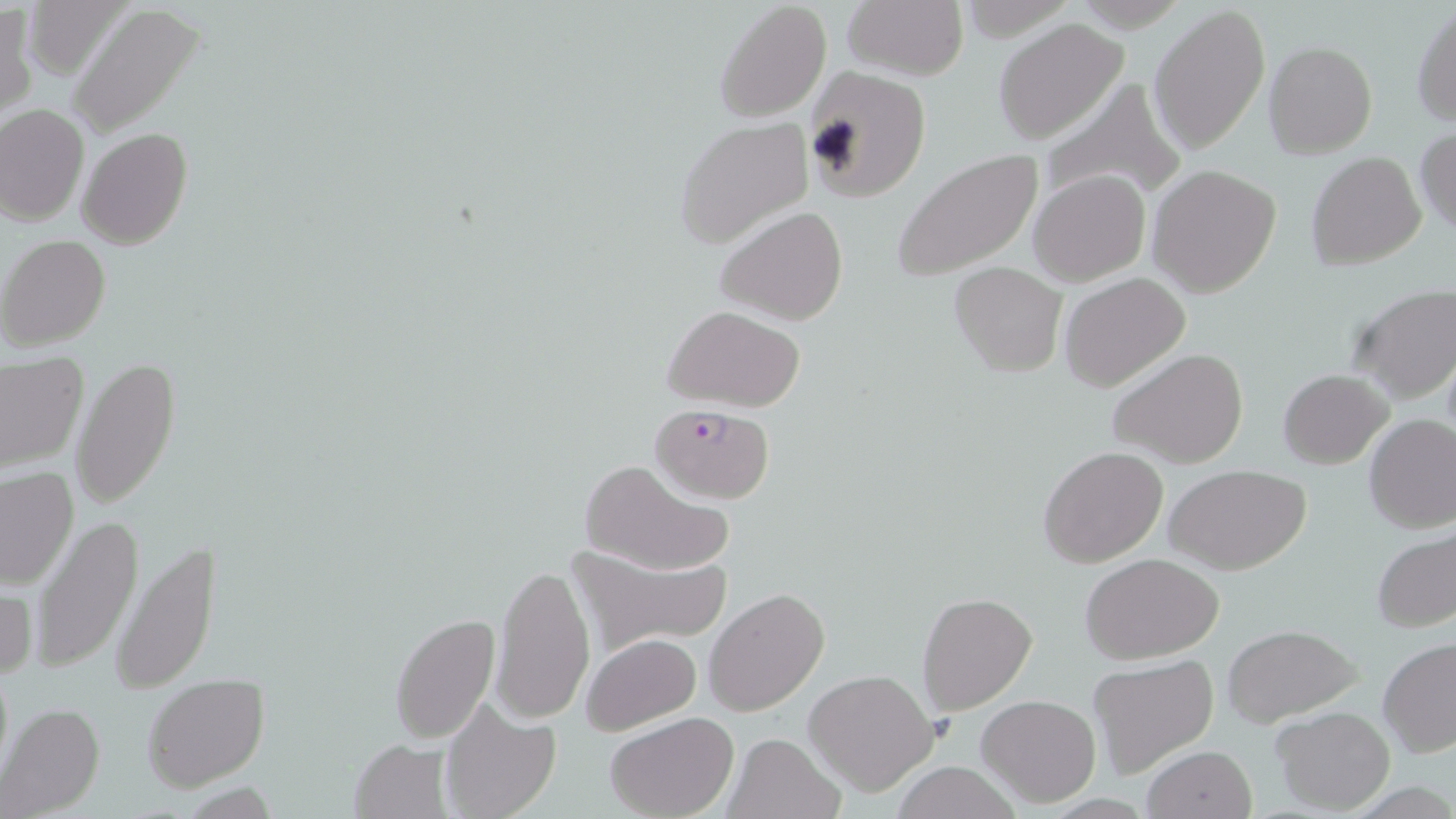

Summary:
  - Coordinate format: approximate bounding boxes as (x1,y1)-(x2,y2) corner pairs in pixels
  - Plasmodium falciparum-infected red blood cell locations: (651,403)-(776,503)
  - Uninfected red blood cell locations: (714,0)-(832,120), (842,1)-(968,81), (1150,3)-(1270,156), (1,4)-(35,122), (68,4)-(205,138), (1411,5)-(1456,126), (992,18)-(1129,144), (1263,41)-(1377,159), (799,66)-(931,204), (1033,76)-(1189,208), (0,104)-(88,224), (675,117)-(815,252), (1414,126)-(1456,237), (78,127)-(193,249), (892,149)-(1044,282), (1306,152)-(1427,270), (1147,164)-(1282,297), (1027,171)-(1151,285), (716,205)-(848,325), (1,236)-(112,352), (949,262)-(1066,378), (1059,273)-(1192,393), (1345,283)-(1456,404), (663,305)-(807,411), (1107,347)-(1250,469), (0,355)-(87,473), (72,358)-(179,510), (1277,369)-(1392,468), (1363,413)-(1456,533), (1038,446)-(1168,569), (574,459)-(734,577), (1165,465)-(1311,575), (0,466)-(79,590), (28,515)-(144,675), (1372,526)-(1454,633), (112,537)-(220,694), (564,543)-(727,657), (1080,553)-(1224,662), (491,561)-(596,724), (0,580)-(37,683), (704,588)-(829,718), (915,592)-(1038,714), (388,613)-(500,742), (1223,625)-(1363,728), (582,634)-(701,734), (1377,637)-(1456,759), (1086,654)-(1218,775), (803,669)-(940,796), (143,675)-(270,792), (975,694)-(1101,807), (438,702)-(561,819), (1,703)-(106,816), (1272,706)-(1395,813), (607,713)-(737,819), (722,731)-(844,819), (349,737)-(453,818), (1140,745)-(1257,819), (889,762)-(1025,819)
  - Slide-level diagnosis: Plasmodium falciparum
  - Preparation: thin blood film
  - Modality: light microscopy
  - Stain: May-Grünwald-Giemsa
  - Field of view: single
  - Magnification: 1000x
  - Image size: 1456×819 pixels